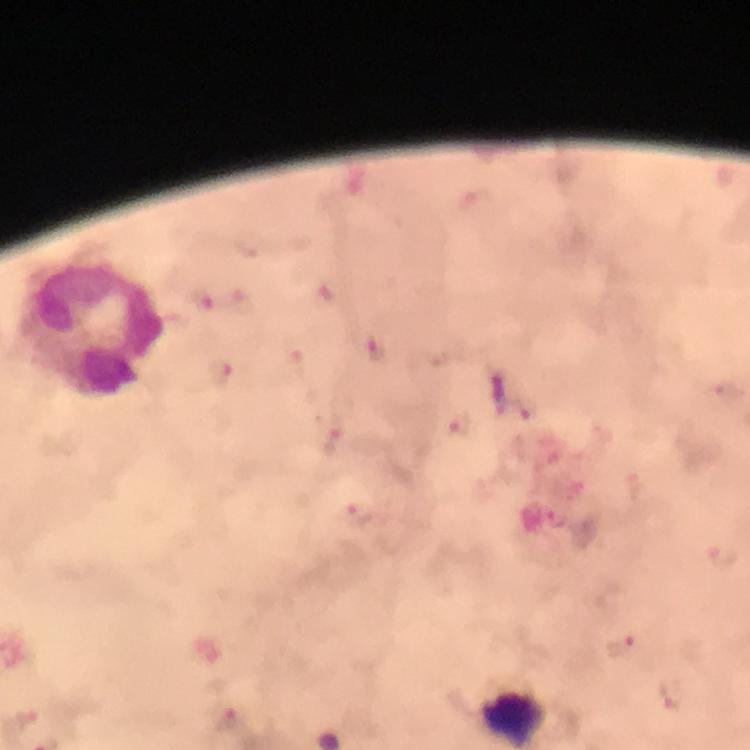
Approximate centers as (x, y) in pixels. Leukocyte locations: (93, 331). Plasmodium parasite locations: (204, 299), (222, 372), (461, 426), (360, 512). Immersion oil was used. From a diagnostic examination for malaria. Giemsa-stained preparation. Thick blood film. Photographed with a smartphone mounted on the microscope. Cropped region of a single field of view. Image is 750×750 pixels. At 100x magnification.